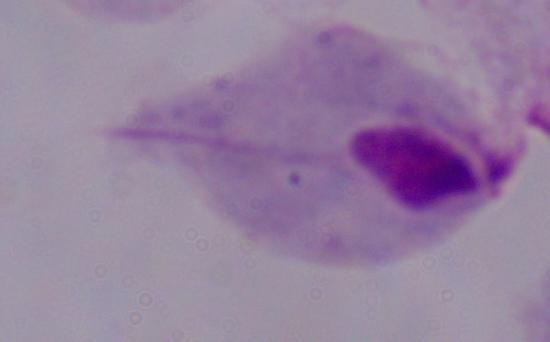
Summary:
  - Magnification: 1000x
  - Identification: trichomonad
  - Modality: photomicrograph